Report the malaria status of this cell.
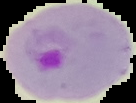

It is parasitized.

From a thin blood film. Segmented cell region on a black background. Image is 136×103 pixels.